Assess the morphology of the erythrocytes.
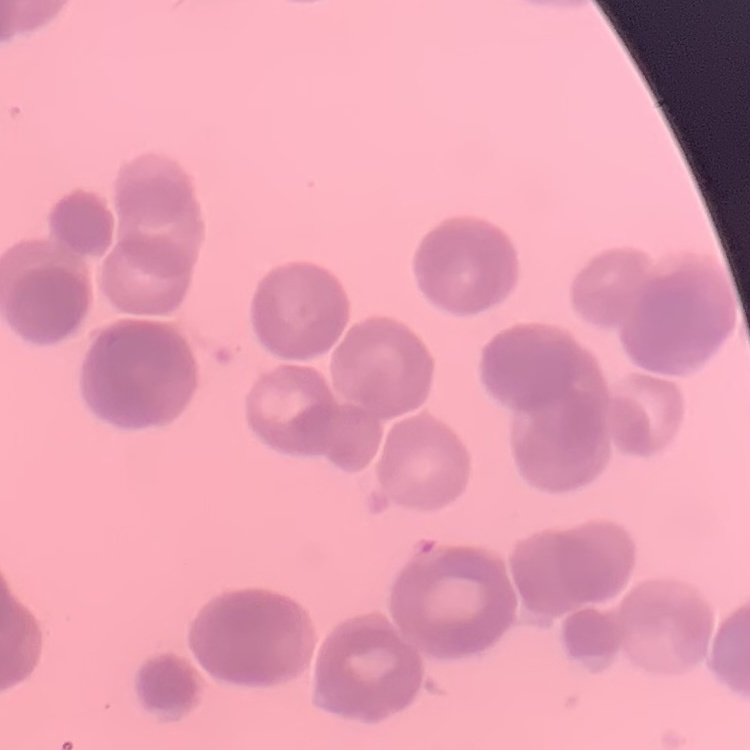

They show rouleaux formation.

Square crop of a larger photomicrograph. Thin blood smear. Field's or Giemsa stain.